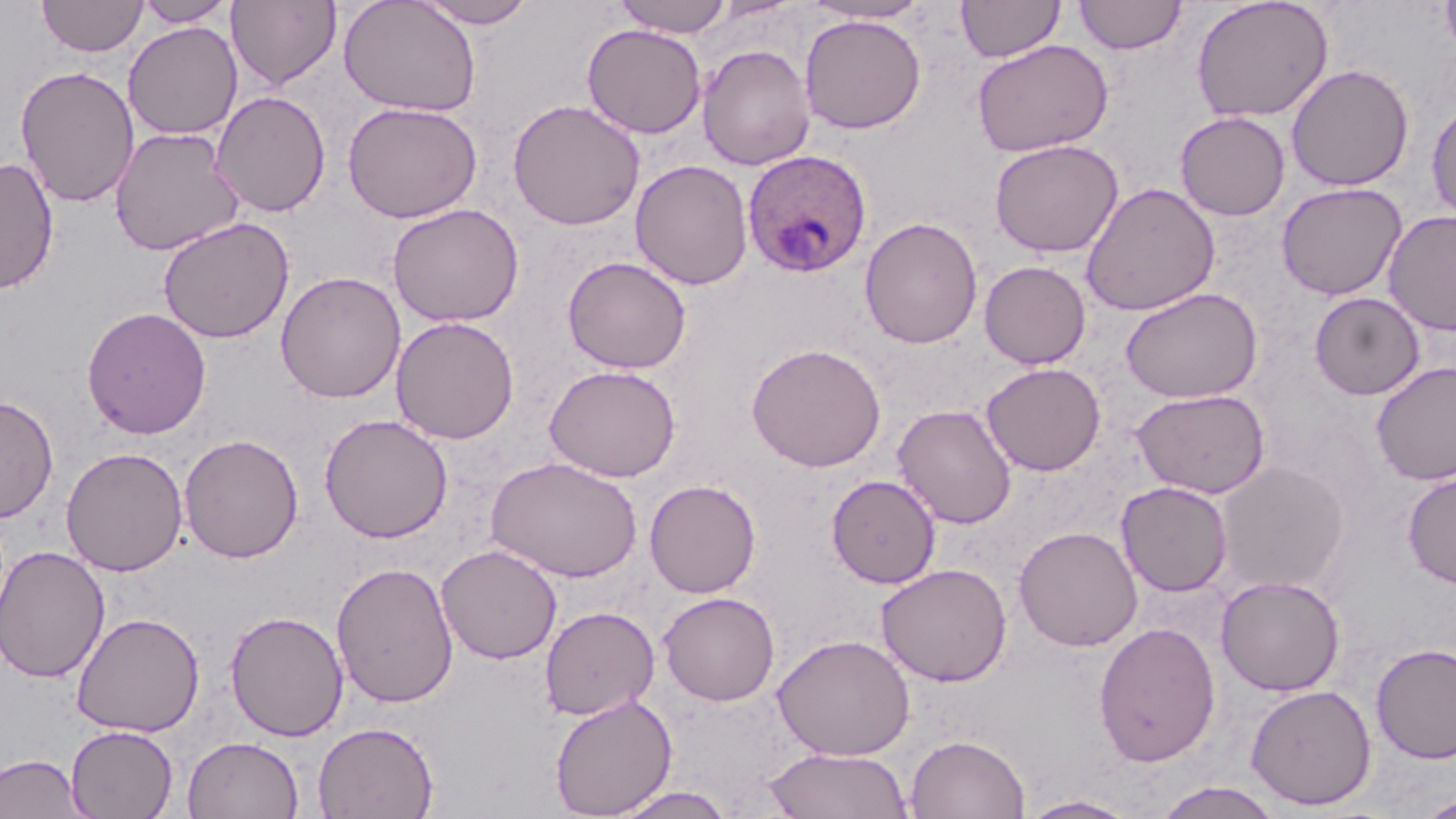 Approximate bounding boxes as (x1,y1)-(x2,y2) corner pairs in pixels. Plasmodium ovale-infected red blood cell locations: (742,149)-(872,277). Uninfected red blood cell locations: (37,0)-(147,57), (134,0)-(236,27), (227,0)-(342,91), (339,0)-(482,117), (413,0)-(539,28), (613,0)-(733,38), (956,0)-(1066,62), (1074,0)-(1188,55), (1191,0)-(1334,123), (1440,0)-(1456,59), (802,1)-(931,24), (799,14)-(926,134), (122,22)-(243,140), (582,23)-(707,139), (972,39)-(1114,157), (697,44)-(815,170), (1286,63)-(1414,192), (15,65)-(140,208), (210,91)-(331,217), (1426,98)-(1456,223), (507,99)-(645,231), (342,101)-(483,223), (1175,111)-(1291,221), (109,127)-(246,257), (988,138)-(1124,257), (0,157)-(59,295), (630,160)-(753,290), (1080,182)-(1220,316), (1274,182)-(1408,300), (387,203)-(525,327), (1383,210)-(1456,336), (157,217)-(294,344), (860,217)-(982,349), (562,255)-(692,374), (979,260)-(1091,369), (275,271)-(406,403), (1120,287)-(1263,403), (1309,292)-(1425,400), (81,306)-(212,440), (390,315)-(520,445), (746,343)-(886,472), (1371,361)-(1456,485), (981,362)-(1106,476), (544,364)-(681,482), (1131,389)-(1271,498), (0,394)-(59,523), (892,403)-(1018,529), (318,413)-(453,543), (178,433)-(304,564), (60,446)-(188,577), (486,455)-(643,582), (1211,459)-(1350,595), (1402,472)-(1456,589), (826,474)-(941,588), (644,479)-(761,598), (1116,481)-(1233,597), (1013,526)-(1143,651), (0,544)-(111,683), (436,544)-(562,664), (331,561)-(459,709), (875,562)-(1012,687), (1216,575)-(1346,696), (658,591)-(780,705), (539,605)-(660,720), (225,610)-(349,742), (71,611)-(205,737), (1093,621)-(1221,767), (773,634)-(916,760), (1371,643)-(1456,764), (1245,683)-(1377,810), (549,694)-(677,818), (313,721)-(439,819), (65,725)-(179,819), (906,733)-(1030,819), (182,736)-(304,819), (763,747)-(915,819), (0,753)-(91,818), (1153,781)-(1285,819), (607,785)-(739,818), (1417,793)-(1456,818), (1018,794)-(1141,818). Slide-level diagnosis: Plasmodium ovale. May-Grünwald-Giemsa stain. Light microscopy. One field of a larger specimen. Image is 1456×819 pixels. 1000x magnification. Thin blood smear.